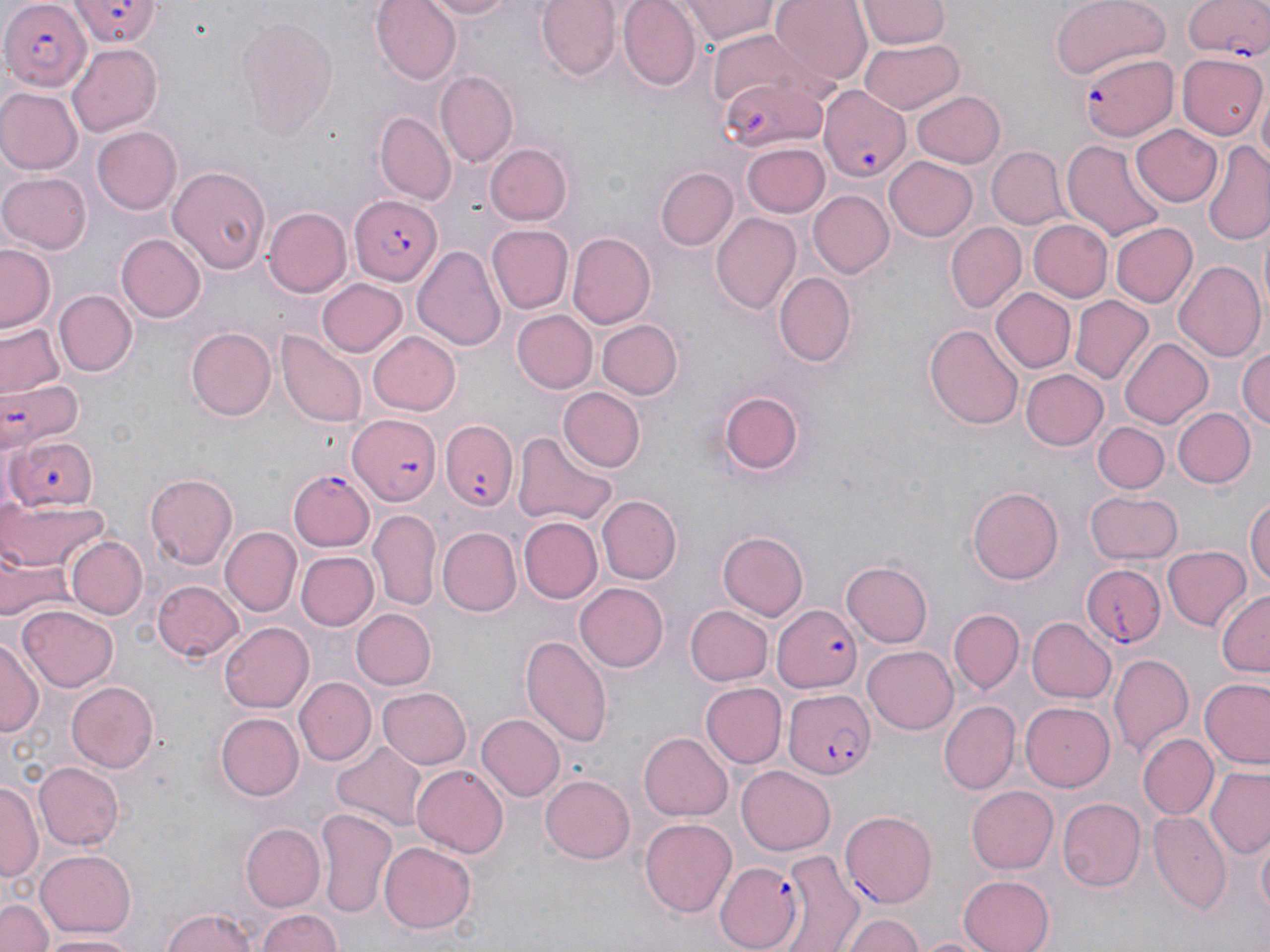
Approximate bounding boxes as (x1, y1, x2, y2) in pixels. Uninfected red blood cell locations: (371, 0, 463, 84), (418, 0, 517, 20), (536, 0, 622, 81), (617, 0, 702, 91), (681, 0, 781, 44), (767, 0, 872, 84), (1050, 0, 1170, 79), (859, 2, 948, 48), (236, 15, 339, 140), (706, 30, 828, 118), (67, 41, 162, 134), (857, 41, 963, 113), (1179, 54, 1266, 140), (437, 70, 517, 167), (1255, 85, 1269, 168), (1, 89, 81, 174), (913, 89, 1006, 168), (376, 113, 456, 202), (1131, 124, 1224, 207), (90, 126, 182, 215), (1062, 138, 1166, 242), (1201, 142, 1270, 245), (486, 143, 572, 225), (742, 143, 829, 217), (987, 146, 1066, 226), (884, 156, 977, 241), (168, 165, 271, 275), (656, 166, 737, 250), (0, 170, 92, 254), (807, 190, 895, 280), (263, 206, 351, 295), (710, 213, 802, 317), (1027, 218, 1114, 303), (946, 222, 1026, 312), (1110, 222, 1196, 308), (487, 224, 572, 312), (567, 232, 655, 329), (117, 233, 205, 322), (1, 243, 58, 334), (413, 243, 505, 353), (1173, 260, 1266, 363), (773, 272, 857, 367), (319, 278, 408, 359), (991, 288, 1076, 373), (57, 290, 136, 375), (1070, 295, 1151, 385), (513, 310, 598, 393), (596, 320, 683, 399), (2, 322, 64, 397), (927, 324, 1023, 432), (185, 327, 275, 420), (366, 329, 460, 416), (279, 332, 365, 428), (1120, 335, 1214, 426), (1237, 344, 1270, 430), (1022, 368, 1109, 451), (717, 386, 809, 478), (560, 387, 645, 470), (1172, 406, 1254, 488), (1095, 421, 1170, 492), (513, 430, 615, 527), (145, 472, 238, 566), (968, 487, 1064, 585), (1087, 490, 1183, 563), (598, 495, 681, 583), (2, 496, 109, 574), (1245, 497, 1270, 593), (369, 508, 442, 610), (519, 517, 602, 605), (220, 526, 301, 615), (439, 527, 521, 615), (719, 530, 807, 621), (66, 536, 147, 620), (1163, 546, 1250, 632), (2, 547, 71, 625), (297, 551, 378, 630), (839, 559, 933, 650), (153, 579, 244, 662), (576, 581, 671, 671), (1215, 588, 1270, 676), (683, 604, 772, 686), (17, 605, 119, 690), (950, 607, 1024, 694), (350, 609, 435, 690), (1026, 616, 1116, 704), (220, 622, 314, 713), (519, 634, 612, 747), (0, 635, 41, 738), (863, 644, 959, 734), (1108, 652, 1194, 757), (296, 678, 374, 767), (1200, 679, 1270, 769), (65, 680, 160, 772), (699, 683, 785, 767), (377, 685, 472, 767), (939, 700, 1019, 793), (1021, 703, 1116, 792), (215, 712, 304, 801), (475, 715, 563, 801), (639, 733, 733, 820), (1139, 733, 1218, 819), (331, 742, 429, 828), (34, 762, 123, 850), (737, 763, 835, 852), (411, 764, 508, 858), (1207, 767, 1269, 858), (541, 773, 636, 864), (2, 780, 40, 882), (967, 786, 1059, 872), (1058, 796, 1146, 893), (316, 809, 399, 920), (1147, 810, 1230, 917), (640, 818, 737, 918), (240, 822, 325, 912), (1254, 834, 1269, 927), (378, 842, 477, 934), (778, 848, 861, 950), (36, 849, 137, 939), (958, 873, 1054, 952), (0, 898, 53, 952), (161, 907, 260, 952), (257, 908, 343, 952), (840, 912, 923, 952), (38, 932, 141, 951), (914, 934, 994, 952). Plasmodium falciparum-infected red blood cell locations: (0, 0, 86, 87), (70, 0, 161, 47), (1181, 0, 1270, 69), (1080, 52, 1178, 140), (722, 76, 826, 155), (817, 83, 913, 187), (350, 195, 442, 287), (1, 376, 83, 452), (346, 415, 442, 506), (443, 420, 519, 512), (10, 437, 98, 513), (290, 468, 375, 551), (1077, 564, 1166, 650), (773, 605, 863, 689), (784, 687, 875, 779), (841, 808, 938, 906), (714, 861, 806, 949). Slide-level diagnosis: Plasmodium falciparum. Thin blood film. Captured at 1000x magnification. Light microscopy. May-Grünwald-Giemsa-stained preparation. One field of a larger specimen. Image is 1270×952 pixels.